Locate every leukocyte (white blood cell).
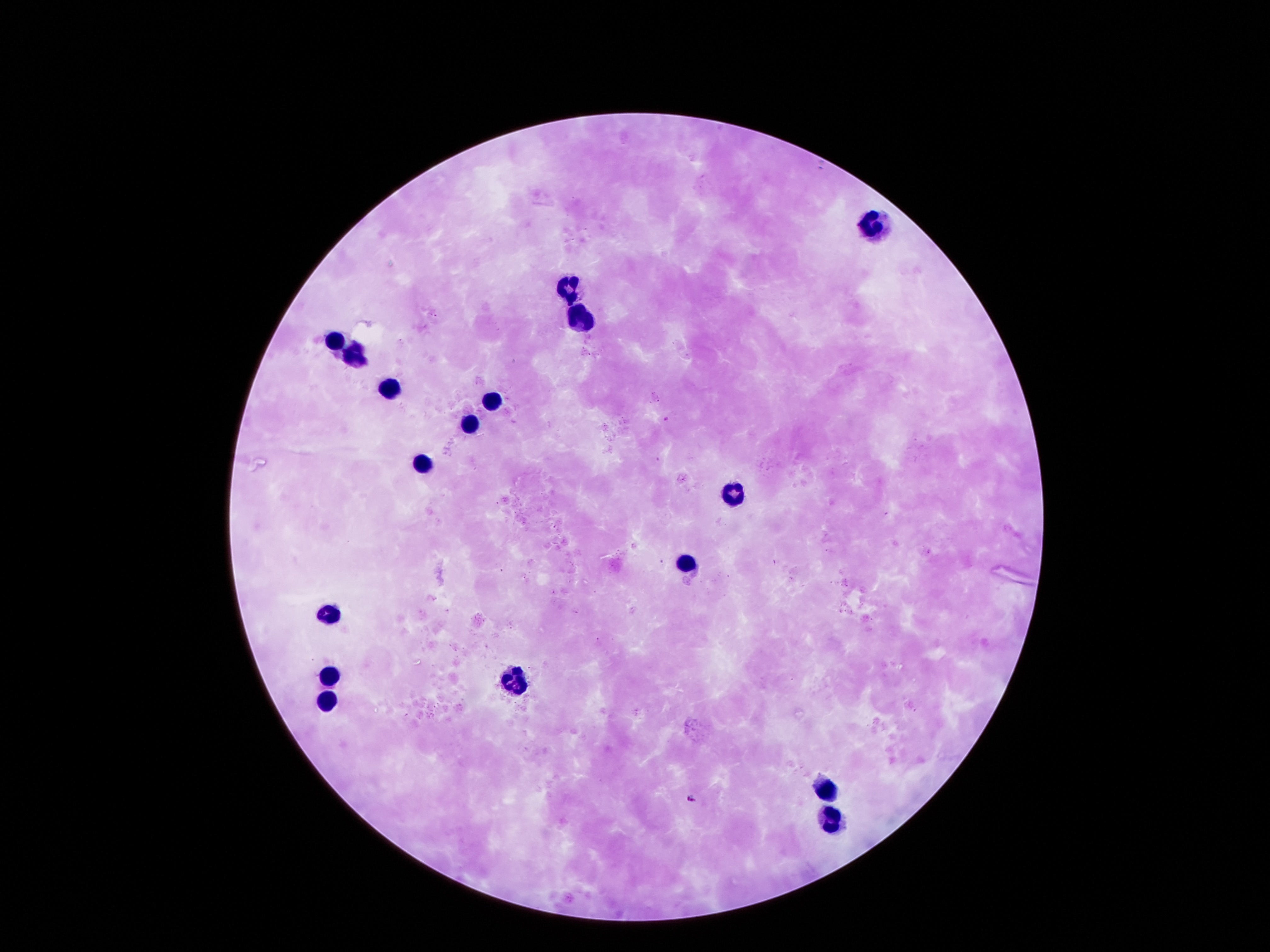

Approximate centers as {x, y} in pixels.
Leukocytes: {877, 226}, {568, 283}, {575, 317}, {336, 340}, {353, 357}, {390, 387}, {491, 398}, {467, 418}, {420, 464}, {733, 488}, {689, 559}, {323, 609}, {326, 673}, {511, 679}, {323, 700}, {824, 784}, {830, 827}.

{
  "patient_malaria_status": "negative",
  "preparation": "thick blood film",
  "image_size": "1270×952 pixels",
  "field_of_view": "one from this slide",
  "stain": "Giemsa",
  "capture": "smartphone camera through the microscope eyepiece",
  "magnification": "100x"
}